Comment on the morphology of the red blood cells.
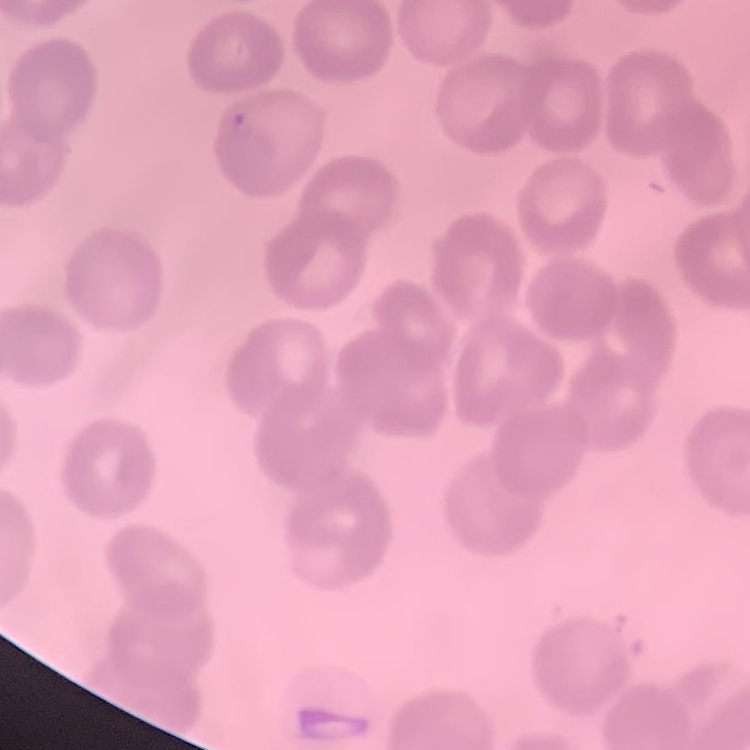
They show no rouleaux formation.

One tile cut from a larger photomicrograph. Field's or Giemsa stain. Thin peripheral smear.